State which parasite is depicted.
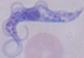

This is a trypanosome.

Summary:
  - Modality: photomicrograph
  - Magnification: 1000x